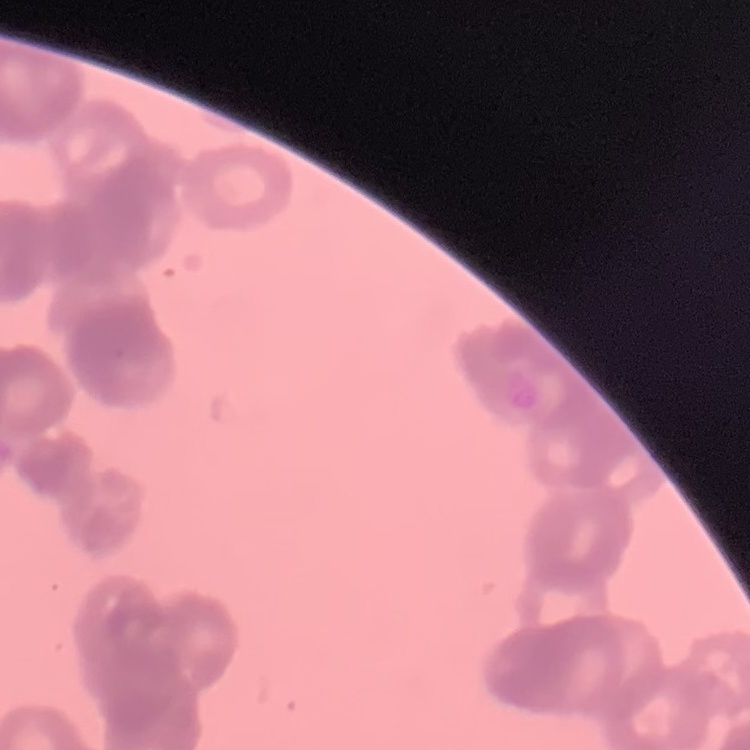
Summary:
  - Erythrocyte morphology: rouleaux formation
  - Stain: Field's or Giemsa
  - Image type: one tile cut from a larger photomicrograph
  - Preparation: thin peripheral smear